Identify the blood parasite species.
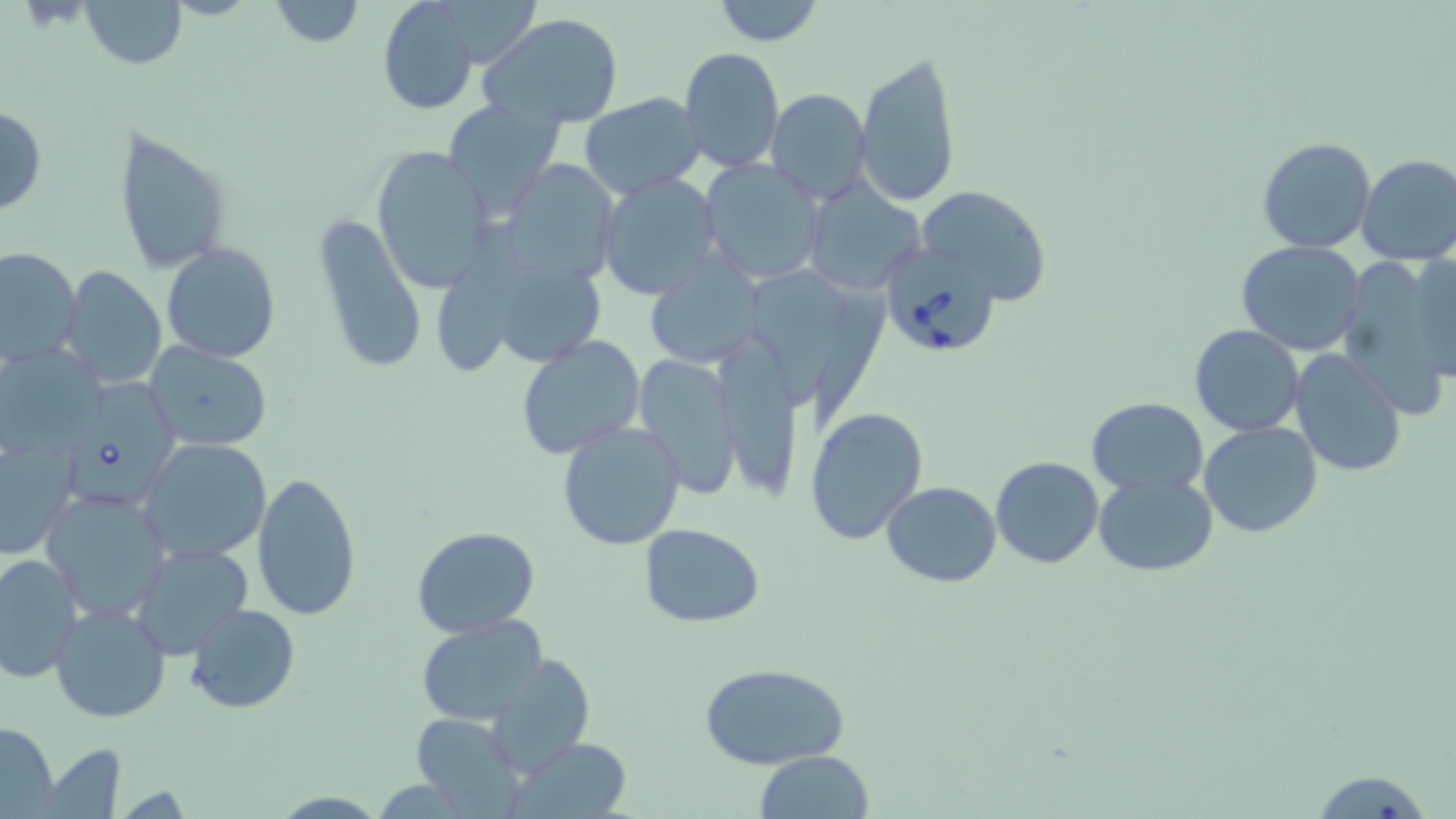
Babesia divergens.

preparation = thin blood smear
field of view = one of a larger specimen
Babesia divergens-infected red blood cell locations = approximate bounding boxes as (x1,y1)-(x2,y2) corner pairs in pixels: (879,241)-(1001,358), (68,377)-(188,503)
uninfected red blood cell locations = approximate bounding boxes as (x1,y1)-(x2,y2) corner pairs in pixels: (80,0)-(188,69), (377,0)-(480,115), (710,0)-(825,47), (267,1)-(364,49), (480,12)-(624,127), (680,47)-(785,175), (854,48)-(962,209), (767,90)-(873,205), (578,92)-(705,198), (442,99)-(565,214), (0,107)-(48,216), (113,127)-(233,273), (1258,137)-(1378,254), (370,146)-(497,294), (1355,153)-(1456,266), (697,158)-(828,286), (502,160)-(622,286), (596,173)-(724,302), (802,182)-(922,293), (916,186)-(1053,304), (314,213)-(427,376), (1235,240)-(1366,355), (162,242)-(281,363), (0,248)-(82,368), (1413,249)-(1456,386), (1334,252)-(1451,415), (644,253)-(764,369), (61,266)-(167,389), (757,269)-(851,398), (1189,324)-(1304,436), (709,333)-(804,499), (515,335)-(647,461), (144,343)-(272,452), (1289,348)-(1407,477), (1,352)-(106,452), (632,353)-(743,499), (1086,398)-(1208,495), (806,407)-(929,547), (557,421)-(687,552), (1199,421)-(1322,538), (0,433)-(81,560), (139,439)-(271,563), (991,455)-(1104,569), (251,468)-(362,621), (1092,471)-(1218,577), (881,482)-(1002,586), (39,488)-(172,621), (640,523)-(766,627), (411,527)-(541,640), (128,543)-(253,658), (0,552)-(83,684), (46,602)-(171,724), (186,603)-(300,714), (414,614)-(548,727), (486,653)-(595,777), (699,662)-(852,767), (407,710)-(522,811), (0,721)-(60,816), (510,737)-(634,818), (43,741)-(127,817), (754,751)-(875,818), (1303,767)-(1437,817)
stain = May-Grünwald-Giemsa
magnification = 1000x
image size = 1456×819 pixels
modality = optical microscopy